Identify the parasite.
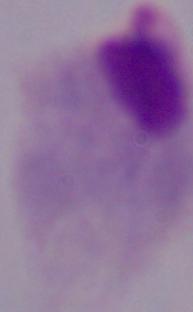

This is a trichomonad.

Summary:
  - Modality: micrograph
  - Magnification: 1000x